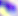
identification: Toxoplasma gondii
magnification: 400x
modality: photomicrograph